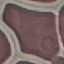

{
  "malaria_status": "uninfected",
  "preparation": "thin blood smear",
  "image_type": "automatically extracted cell patch, resized to 64 × 64 pixels",
  "capture": "smartphone camera at the microscope eyepiece",
  "stain": "Giemsa"
}